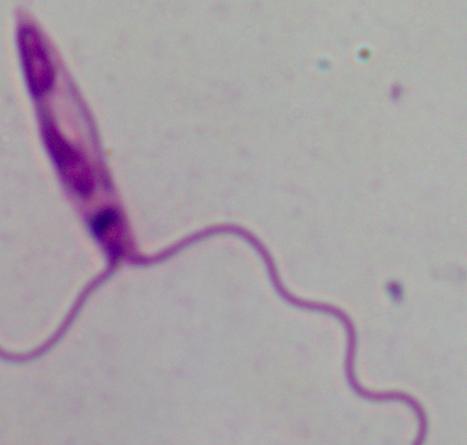
Summary:
  - Modality: micrograph
  - Identification: Leishmania
  - Magnification: 1000x